Give the position of every leukocyte visible.
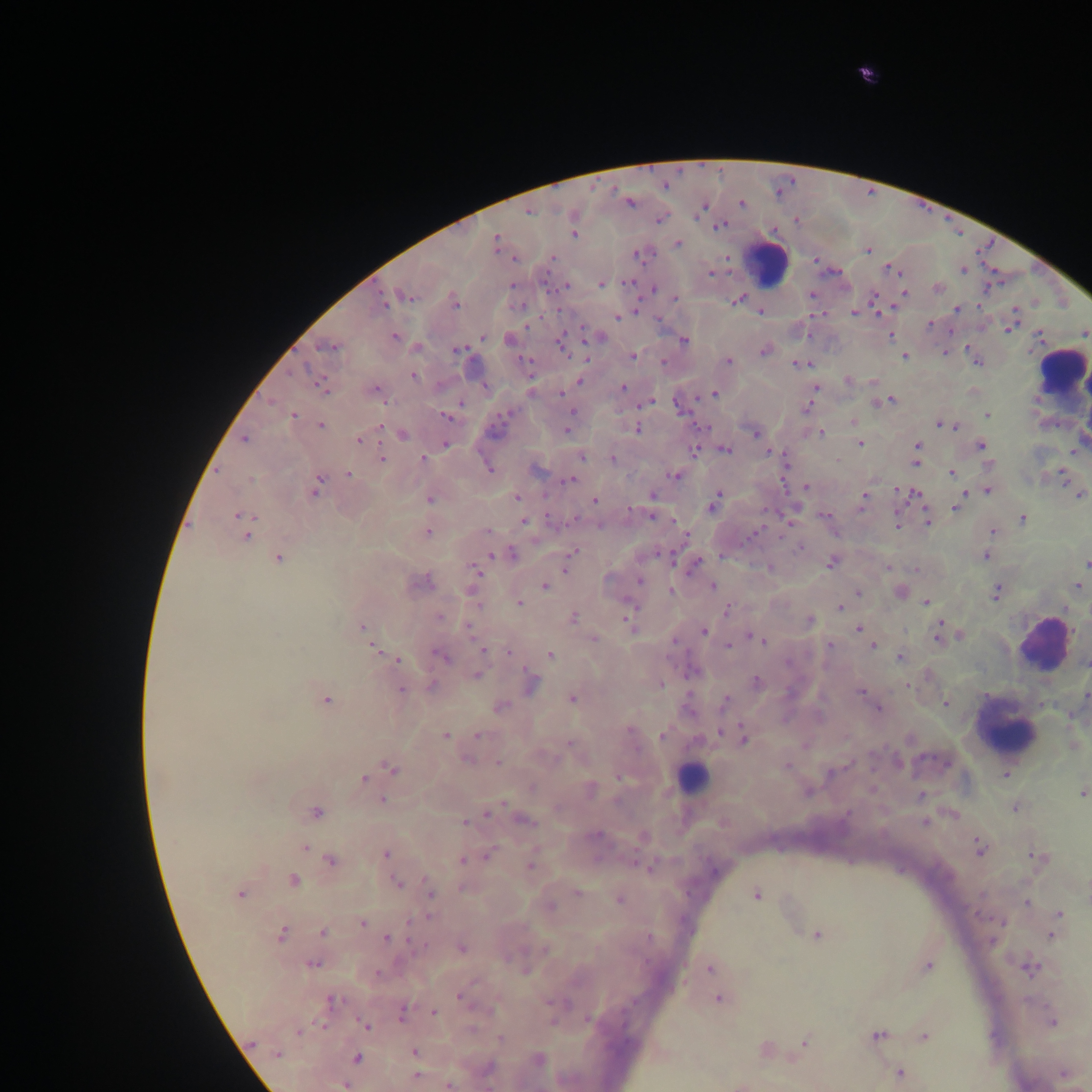
Approximate centers as (x, y) in pixels.
Leukocytes: (766, 262), (1061, 373), (1043, 646), (1005, 728), (691, 778).

Plasmodium parasite locations: (867, 75), (629, 201), (741, 203), (704, 206), (528, 210), (658, 219), (573, 223), (719, 225), (573, 234), (496, 242), (677, 244), (868, 249), (637, 254), (552, 257), (816, 259), (890, 268), (964, 269), (710, 273), (601, 283), (565, 286), (653, 288), (938, 288), (904, 292), (811, 295), (406, 296), (674, 298), (736, 299), (875, 300), (453, 301), (384, 302), (957, 308), (760, 310), (854, 312), (617, 317), (931, 324), (1008, 328), (1084, 332), (889, 335), (395, 336), (482, 336), (596, 337), (508, 339), (683, 341), (561, 342), (331, 346), (417, 347), (458, 349), (764, 350), (945, 351), (904, 355), (632, 356), (728, 360), (977, 361), (800, 363), (413, 376), (847, 380), (580, 381), (321, 385), (622, 387), (816, 388), (374, 389), (713, 394), (886, 401), (646, 402), (680, 405), (809, 406), (572, 414), (988, 414), (292, 415), (447, 416), (853, 421), (940, 424), (321, 425), (953, 426), (636, 428), (567, 429), (820, 432), (755, 433), (402, 434), (245, 439), (359, 440), (860, 443), (445, 444), (980, 446), (917, 448), (695, 449), (725, 450), (769, 451), (582, 456), (383, 458), (613, 458), (423, 459), (784, 459), (916, 459), (489, 468), (952, 472), (348, 474), (676, 475), (1061, 475), (569, 479), (316, 485), (806, 487), (897, 490), (988, 490), (915, 493), (652, 494), (965, 494), (1080, 494), (518, 497), (961, 498), (429, 499), (864, 499), (594, 501), (714, 503), (956, 507), (652, 514), (824, 515), (241, 516), (790, 516), (897, 518), (1022, 519), (524, 520), (928, 521), (896, 524), (487, 531), (992, 531), (427, 532), (246, 534), (801, 547), (571, 553), (511, 554), (664, 555), (985, 556), (277, 558), (831, 561), (568, 563), (694, 564), (1086, 564), (888, 567), (475, 569), (640, 580), (420, 582), (1077, 585), (544, 586), (712, 586), (671, 591), (997, 591), (857, 592), (901, 592), (926, 602), (519, 603), (840, 607), (728, 609), (439, 617), (572, 617), (630, 617), (808, 620), (362, 627), (469, 628), (858, 628), (703, 630), (863, 631), (939, 632), (960, 635), (593, 639), (759, 639), (728, 645), (873, 645), (830, 646), (375, 649), (483, 649), (509, 652), (441, 655), (550, 655), (901, 657), (398, 659), (692, 671), (476, 675), (529, 682), (757, 682), (660, 684), (431, 686), (401, 689), (861, 691), (1086, 695), (571, 698), (325, 699), (869, 699), (724, 700), (946, 703), (499, 707), (878, 708), (477, 735), (662, 735), (445, 736), (743, 737), (467, 759), (897, 761), (498, 762), (786, 766), (391, 767), (1005, 774), (363, 779), (589, 788), (808, 790), (1083, 792), (922, 795), (383, 799), (1015, 807), (489, 811), (316, 812), (523, 820), (925, 822), (467, 823), (643, 836), (305, 847), (979, 847), (385, 854), (487, 855), (1038, 857), (330, 860), (462, 860), (530, 864), (646, 865), (292, 881), (396, 883), (430, 891), (240, 893), (578, 893), (757, 895), (620, 898), (1027, 902), (549, 906), (1059, 914), (1055, 922), (362, 923), (322, 932), (1053, 933), (281, 934), (816, 934), (994, 938), (388, 939), (461, 948), (312, 962), (927, 965), (1029, 967), (709, 968), (460, 995), (719, 997), (331, 1000), (402, 1012), (434, 1013), (1051, 1020), (364, 1025), (299, 1031), (878, 1035), (924, 1037), (805, 1042), (765, 1049), (414, 1052), (277, 1054), (356, 1058), (537, 1060), (488, 1068), (899, 1073), (1063, 1073), (416, 1076), (344, 1084), (447, 1084), (740, 1084). Image is 1092×1092 pixels. Photographed through a microscope with a mobile-phone camera. Thick blood film. One field of view. Collected in Ghana.